Describe the morphology of the red blood cells.
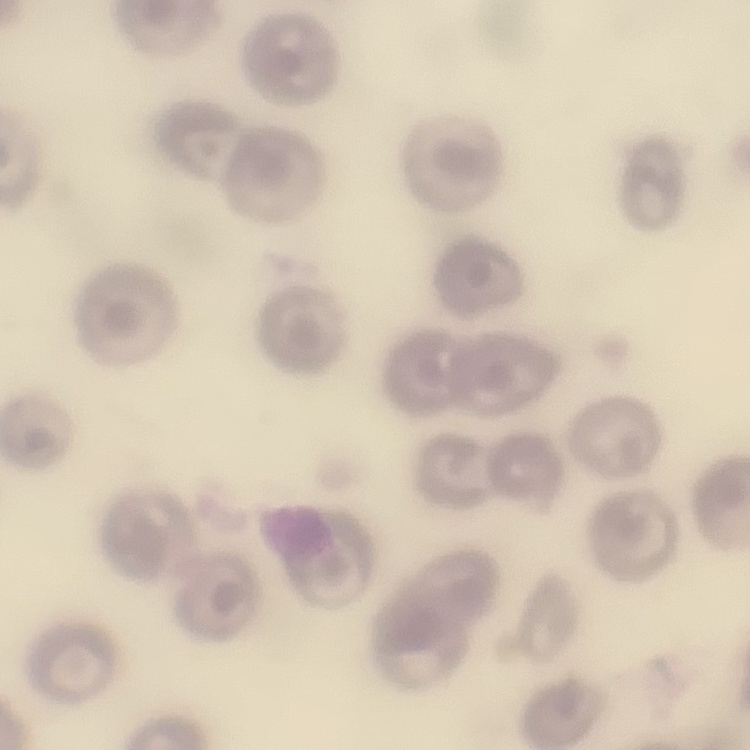

No rouleaux formation.

image type = one tile cut from a larger photomicrograph
preparation = thin peripheral smear
stain = Field's or Giemsa